Give the preparation type.
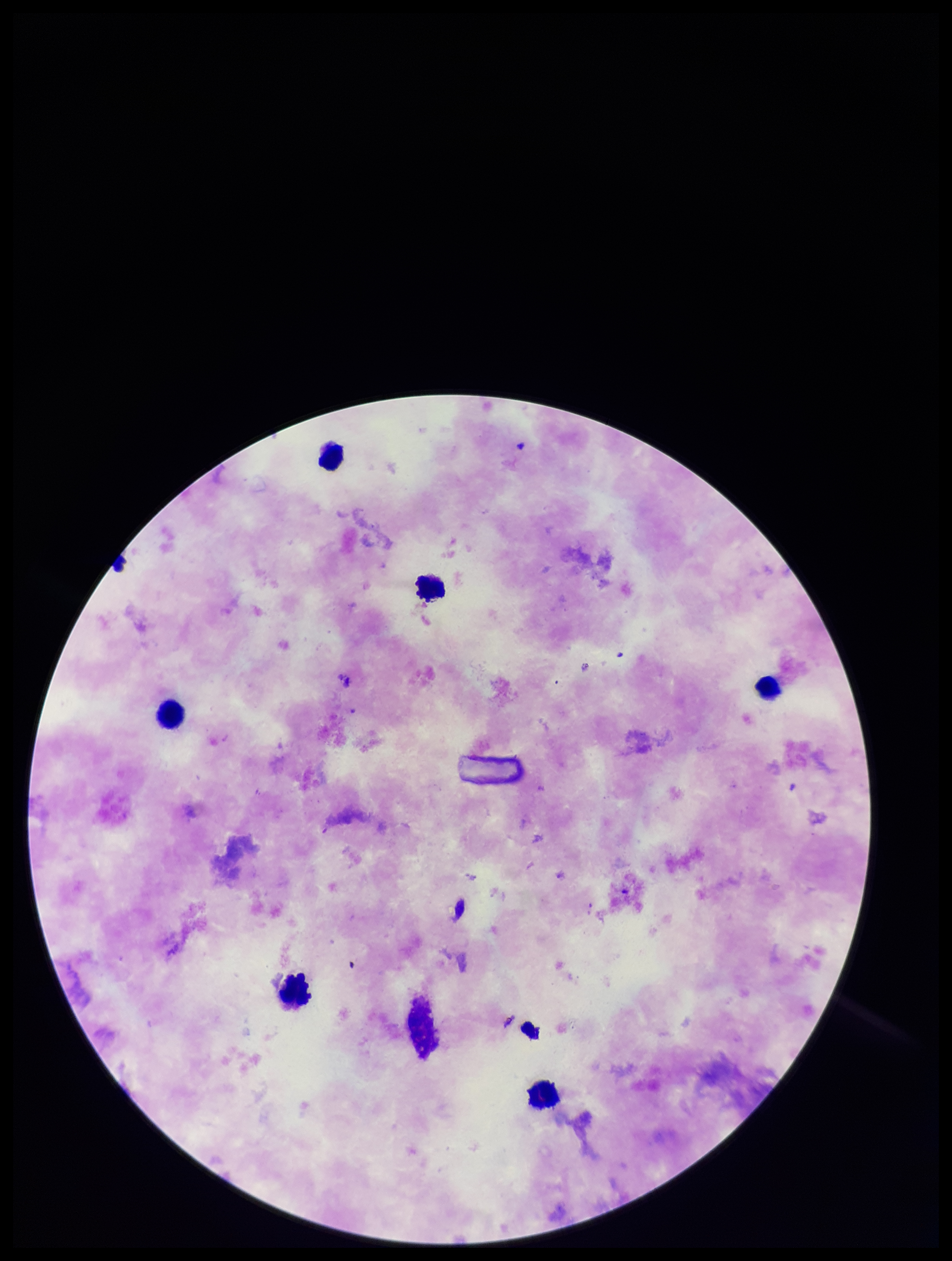

A thick smear.

Summary:
  - Plasmodium parasites: none detected
  - Field of view: single
  - Image size: 952×1261 pixels
  - Parasite count: 0
  - Patient malaria status: negative
  - Capture: smartphone photograph through the microscope eyepiece
  - Leukocyte count: 6
  - Stain: Giemsa